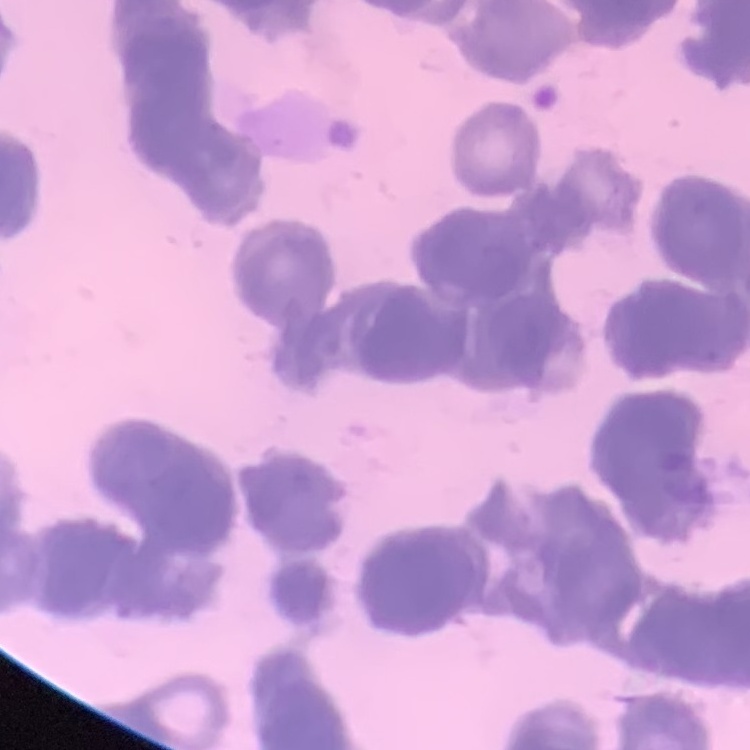
Summary:
  - Erythrocyte morphology: rouleaux formation
  - Stain: Field's or Giemsa
  - Image type: one tile cut from a larger photomicrograph
  - Preparation: thin blood film